Comment on the morphology of the red blood cells.
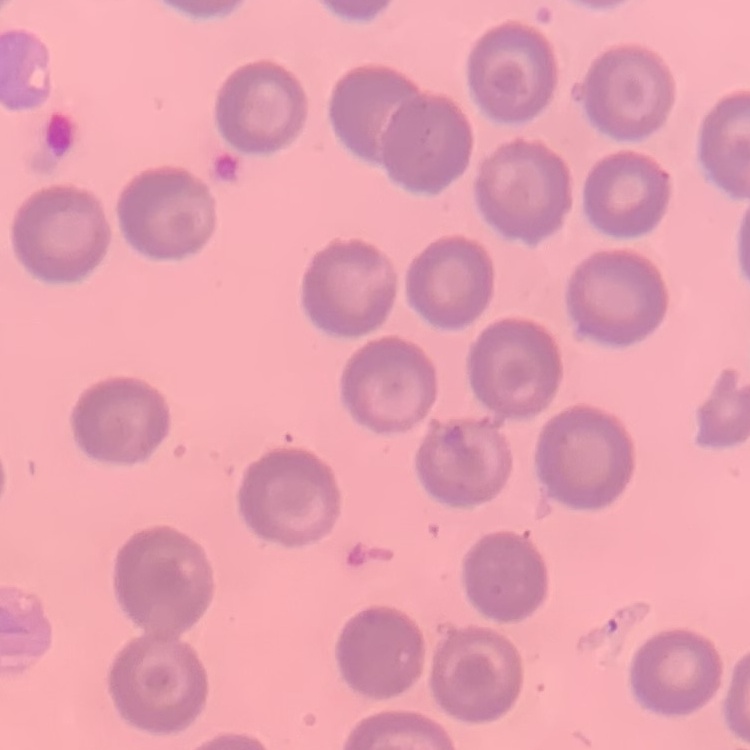
They show no rouleaux formation.

One tile cut from a larger photomicrograph. Thin blood film. Field's or Giemsa stain.